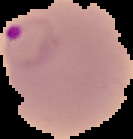
Summary:
  - Malaria status: parasitized
  - Image size: 133×139 pixels
  - Preparation: thin blood film
  - Image type: cell region segmented out of the field of view; surrounding area masked to black